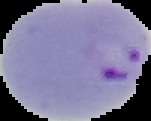
result = malaria parasites identified
image size = 151×121 pixels
preparation = thin blood film
image type = cell region segmented out of the field of view; surrounding area masked to black